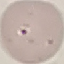 Result: negative for malaria parasites. Acquired by smartphone through the microscope eyepiece. Giemsa stain. Thin blood smear. Cell patch, automatically extracted from a larger field of view and resized to 64 × 64 pixels.